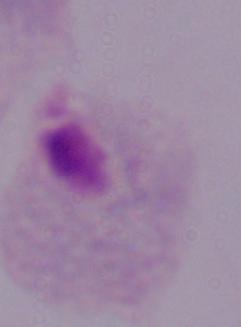
Micrograph. Captured at 1000x magnification. A trichomonad is seen.